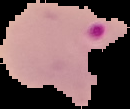
image size = 130×109 pixels
preparation = thin blood smear
image type = segmented cell region with the area outside set to black
malaria status = parasitized